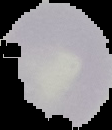

image_size: 112×130 pixels
image_type: segmented cell region on a black background
malaria_status: uninfected
preparation: thin blood film